Outline each blood parasite and name the species.
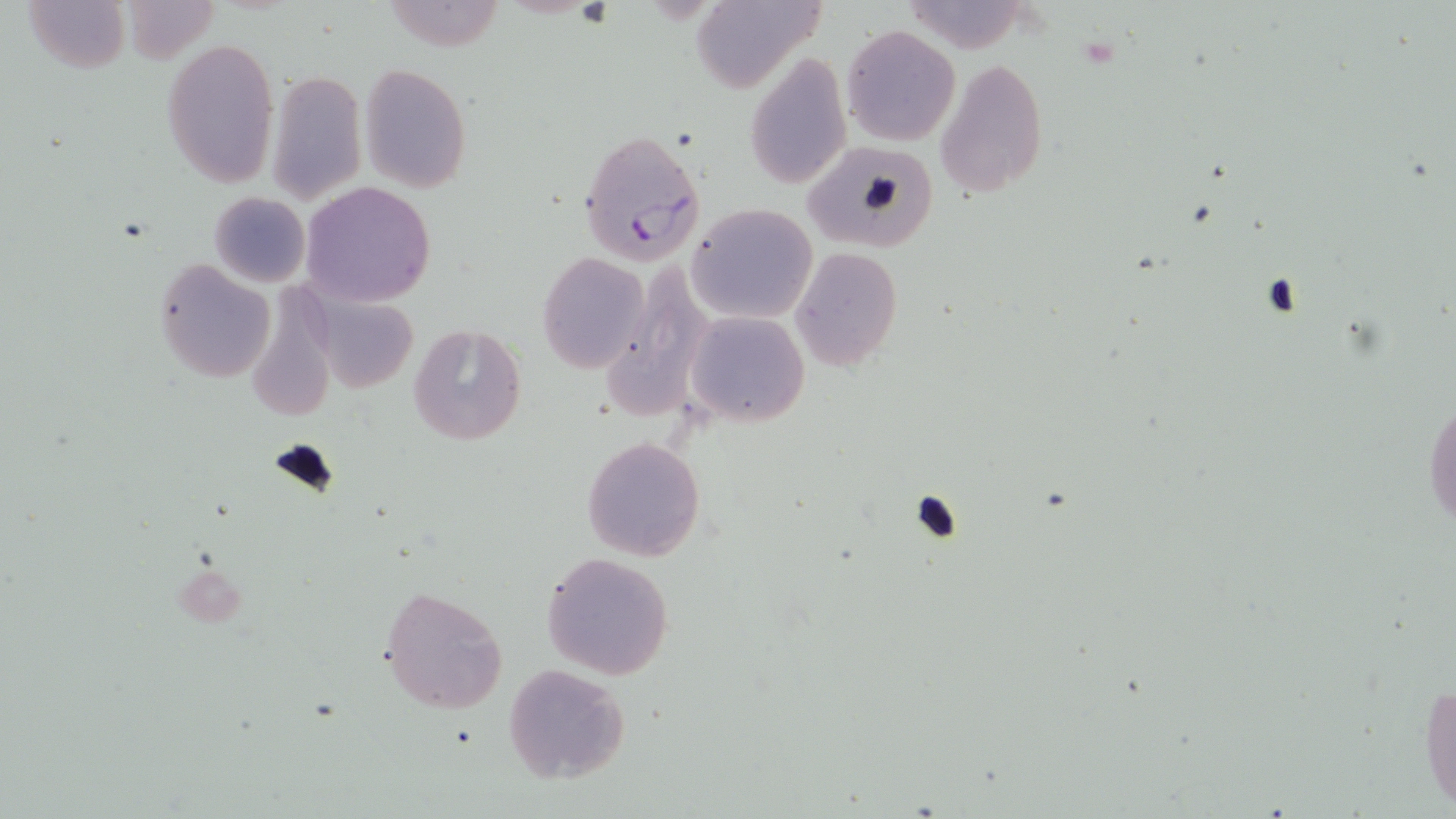

Approximate bounding boxes as named x1/y1/x2/y2 corners in pixels.
Plasmodium falciparum-infected red blood cells: (x1=577, y1=128, x2=706, y2=267).
No Plasmodium ovale, Plasmodium malariae, Plasmodium vivax, Babesia divergens, or Trypanosoma brucei observed.

Summary:
  - Uninfected red blood cell locations: (x1=24, y1=0, x2=130, y2=71), (x1=122, y1=0, x2=217, y2=64), (x1=383, y1=0, x2=506, y2=51), (x1=689, y1=0, x2=825, y2=93), (x1=842, y1=26, x2=959, y2=146), (x1=163, y1=37, x2=279, y2=187), (x1=745, y1=52, x2=849, y2=191), (x1=936, y1=58, x2=1048, y2=198), (x1=359, y1=64, x2=472, y2=193), (x1=268, y1=70, x2=366, y2=203), (x1=801, y1=143, x2=936, y2=255), (x1=302, y1=183, x2=436, y2=307), (x1=208, y1=192, x2=310, y2=288), (x1=688, y1=203, x2=818, y2=322), (x1=791, y1=247, x2=902, y2=370), (x1=537, y1=251, x2=650, y2=375), (x1=153, y1=260, x2=276, y2=384), (x1=611, y1=264, x2=716, y2=417), (x1=239, y1=271, x2=342, y2=418), (x1=312, y1=293, x2=418, y2=391), (x1=686, y1=311, x2=808, y2=427), (x1=407, y1=323, x2=526, y2=445), (x1=1423, y1=378, x2=1455, y2=542), (x1=580, y1=435, x2=707, y2=562), (x1=541, y1=552, x2=674, y2=680), (x1=380, y1=586, x2=508, y2=714), (x1=502, y1=664, x2=631, y2=783), (x1=1419, y1=672, x2=1455, y2=815)
  - Slide-level diagnosis: Plasmodium falciparum
  - Stain: May-Grünwald-Giemsa
  - Field of view: single
  - Modality: optical microscopy
  - Preparation: thin blood smear
  - Image size: 1456×819 pixels
  - Magnification: 1000x